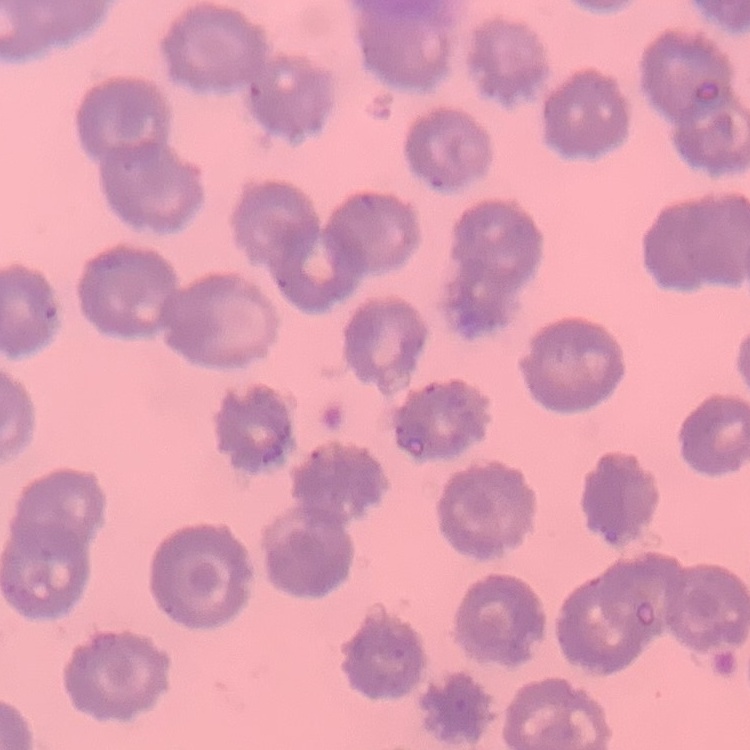
The red blood cells show no rouleaux formation. Square crop of a larger photomicrograph. Thin blood film. Stained with either Field's or Giemsa.